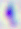 Photomicrograph. Captured at 400x magnification. Toxoplasma gondii is seen.